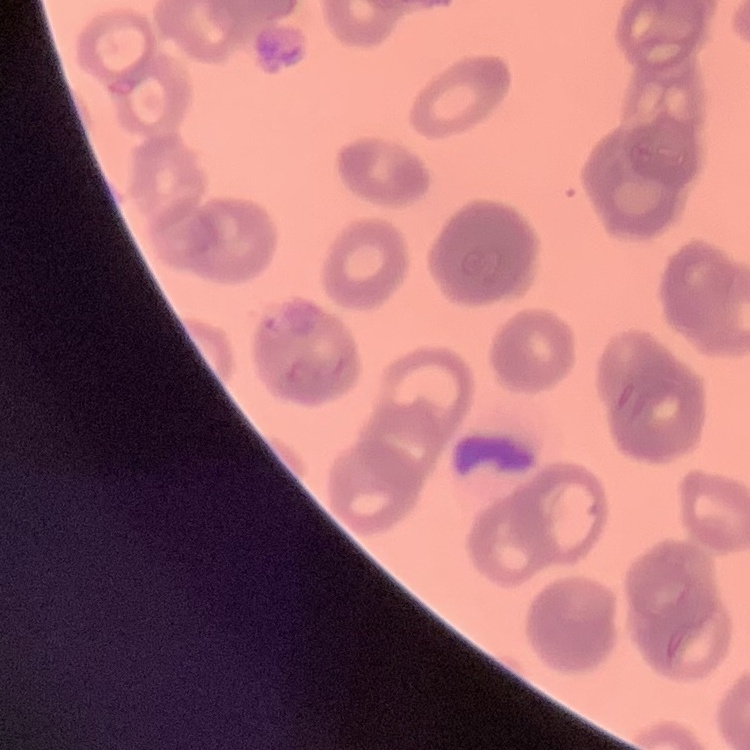
The erythrocytes exhibit rouleaux formation. Thin peripheral smear. Square crop of a larger photomicrograph. Field's or Giemsa stain.